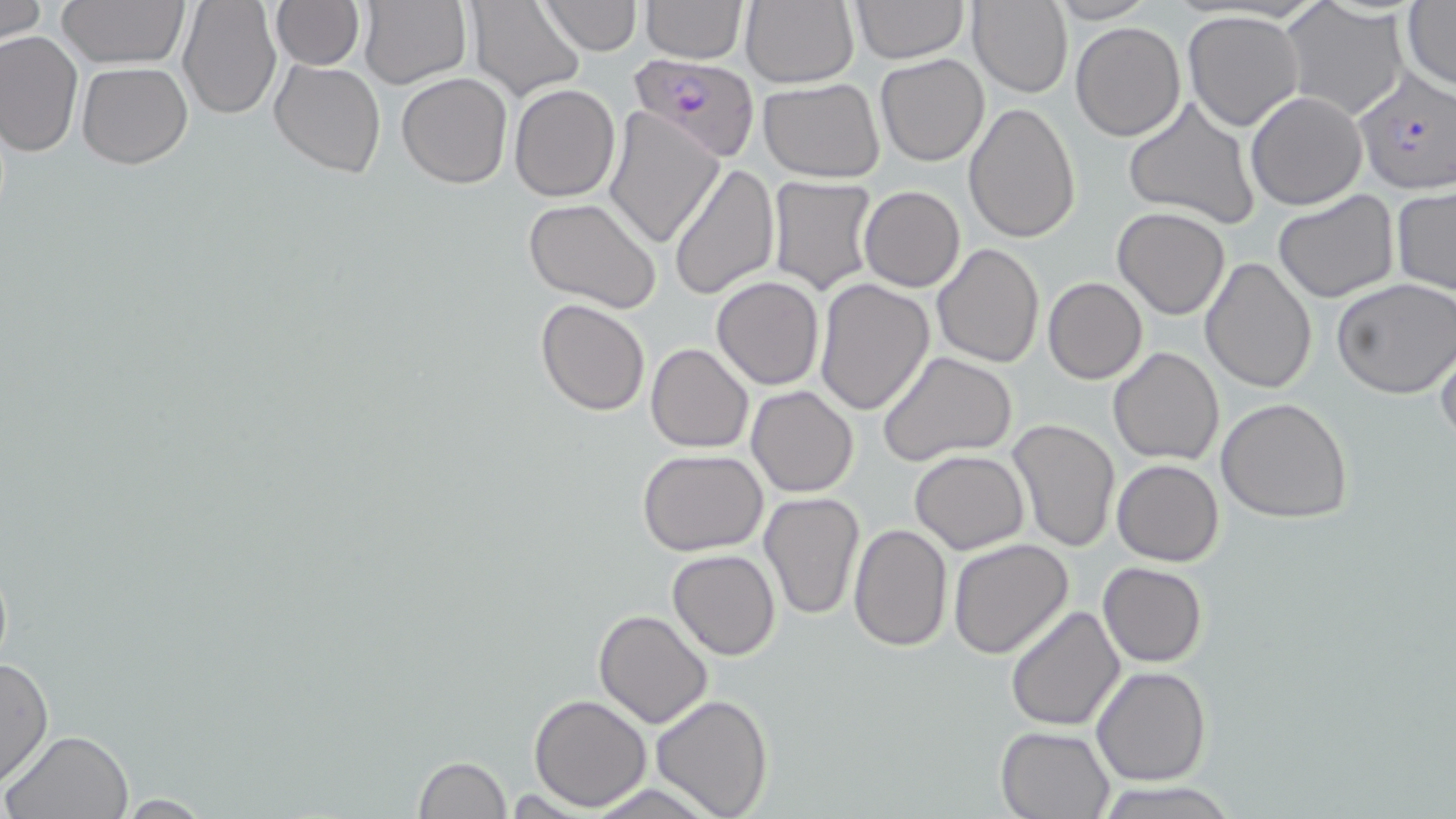

Approximate bounding boxes as (x1,y1)-(x2,y2) corner pairs in pixels. Plasmodium falciparum-infected red blood cell locations: (629,54)-(760,163), (1353,66)-(1456,195). Uninfected red blood cell locations: (0,0)-(47,44), (58,0)-(188,70), (177,0)-(280,119), (269,0)-(364,70), (640,0)-(747,63), (738,0)-(859,89), (848,0)-(970,64), (969,0)-(1072,98), (465,1)-(585,102), (538,1)-(642,54), (1044,1)-(1156,24), (1402,1)-(1456,93), (358,2)-(471,88), (1280,3)-(1409,120), (1182,9)-(1306,131), (1070,20)-(1186,142), (0,31)-(82,159), (875,54)-(990,167), (269,58)-(387,181), (76,61)-(193,168), (396,73)-(513,189), (758,78)-(885,183), (509,83)-(621,202), (1245,91)-(1367,211), (1122,96)-(1262,232), (963,101)-(1082,244), (604,107)-(726,249), (666,162)-(779,301), (766,177)-(881,295), (860,186)-(965,292), (1391,186)-(1456,297), (1272,190)-(1400,306), (522,199)-(662,313), (1113,207)-(1230,320), (932,243)-(1044,368), (1200,255)-(1319,395), (711,276)-(824,390), (813,276)-(935,416), (1043,277)-(1148,384), (1331,278)-(1456,400), (535,299)-(651,417), (1433,328)-(1456,448), (646,343)-(753,452), (1108,345)-(1224,466), (876,350)-(1018,466), (747,386)-(859,497), (1216,397)-(1354,522), (1006,418)-(1121,555), (909,449)-(1029,555), (639,450)-(768,556), (1112,459)-(1224,566), (758,492)-(865,622), (848,522)-(952,651), (948,539)-(1076,659), (666,550)-(780,660), (1098,562)-(1207,667), (1005,606)-(1126,732), (592,608)-(713,729), (0,655)-(53,787), (1092,665)-(1212,785), (528,694)-(651,809), (650,694)-(774,819), (996,726)-(1114,818), (1,728)-(133,818), (411,757)-(511,818), (1091,779)-(1241,818), (109,794)-(220,816). Slide-level diagnosis: Plasmodium falciparum. Captured at 1000x magnification. Single field of view. Light microscopy. Thin blood smear. May-Grünwald-Giemsa stain. Image is 1456×819 pixels.